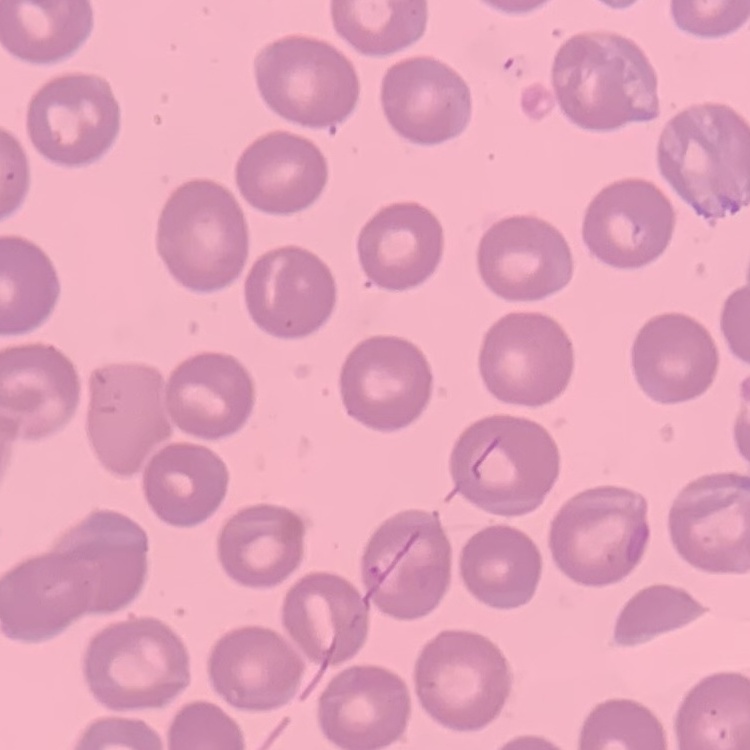

Summary:
  - Red blood cell morphology: no rouleaux formation
  - Stain: Field's or Giemsa
  - Preparation: thin blood film
  - Image type: square crop of a larger photomicrograph